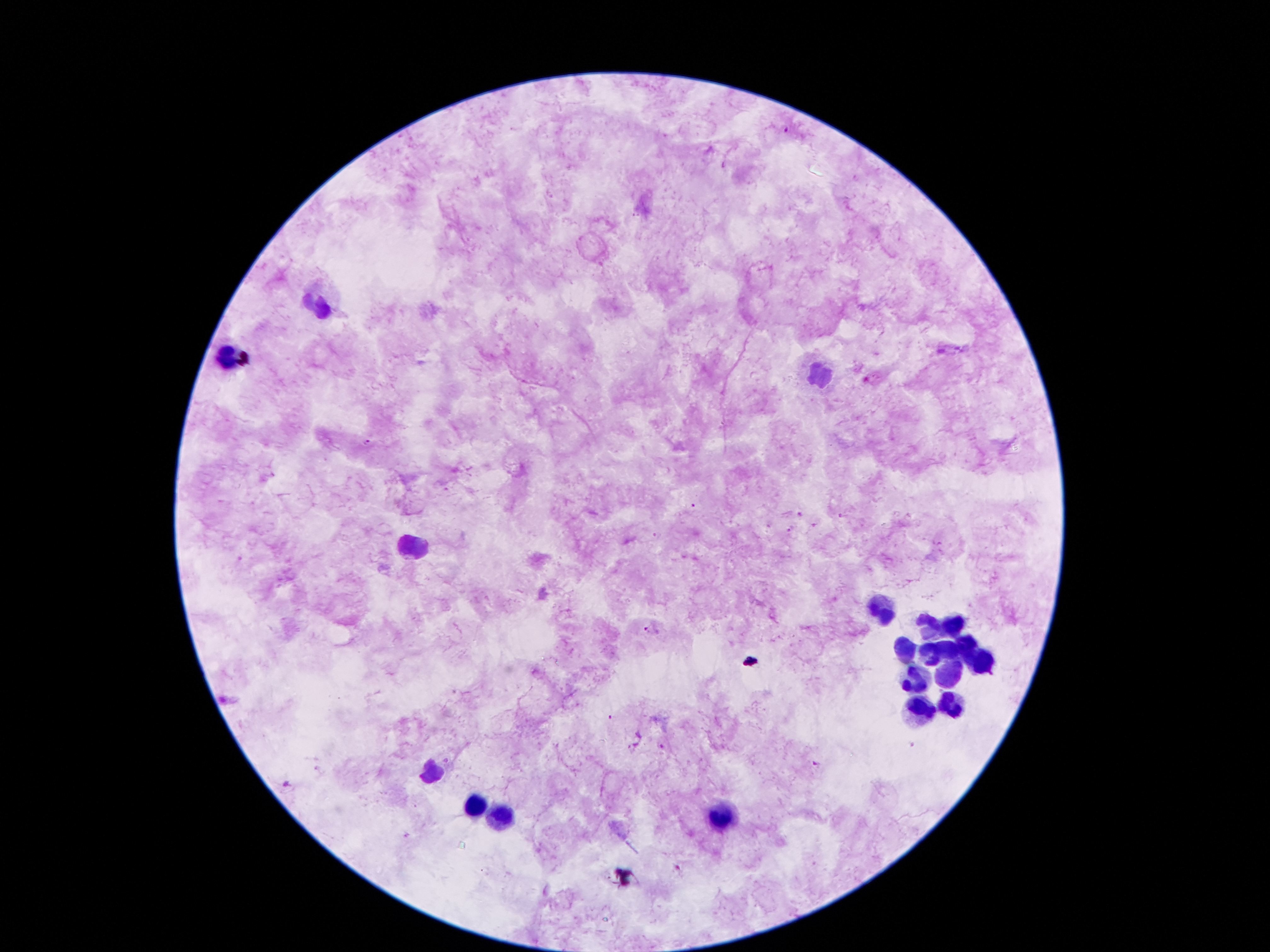
{
  "plasmodium_parasite_locations": "approximate centers as {x, y} in pixels: {786, 127}, {636, 215}, {365, 442}, {691, 507}, {841, 518}, {791, 530}, {656, 535}, {648, 629}, {612, 720}, {910, 745}, {662, 746}, {815, 765}, {288, 784}",
  "leukocyte_locations": "approximate centers as {x, y} in pixels: {318, 306}, {228, 357}, {823, 376}, {411, 547}, {880, 611}, {929, 628}, {953, 628}, {969, 644}, {902, 646}, {949, 648}, {929, 651}, {986, 659}, {951, 677}, {916, 679}, {916, 706}, {949, 710}, {436, 774}, {473, 810}, {721, 816}, {502, 821}",
  "patient_malaria_status": "positive for Plasmodium falciparum",
  "image_size": "1270×952 pixels",
  "stain": "Giemsa",
  "capture": "smartphone camera through the microscope eyepiece",
  "magnification": "100x",
  "preparation": "thick blood film",
  "field_of_view": "single"
}